Comment on the morphology of the erythrocytes.
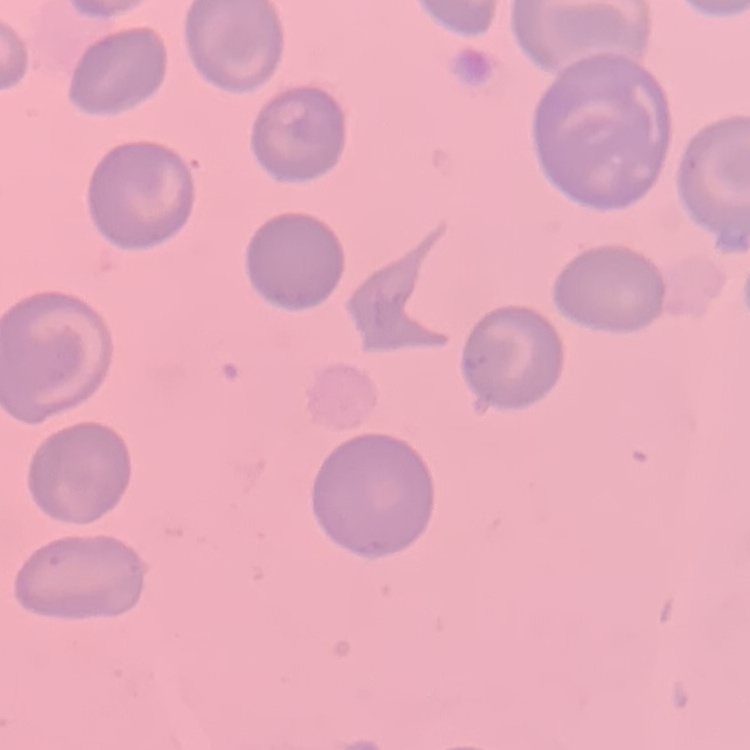
No rouleaux formation.

Summary:
  - Preparation: thin blood film
  - Stain: Field's or Giemsa
  - Image type: square crop of a larger photomicrograph